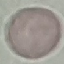

Result: negative for malaria parasites. Giemsa-stained preparation. Cell patch, automatically extracted from a larger field of view and resized to 64 × 64 pixels. Acquired by smartphone through the microscope eyepiece. Thin blood smear.